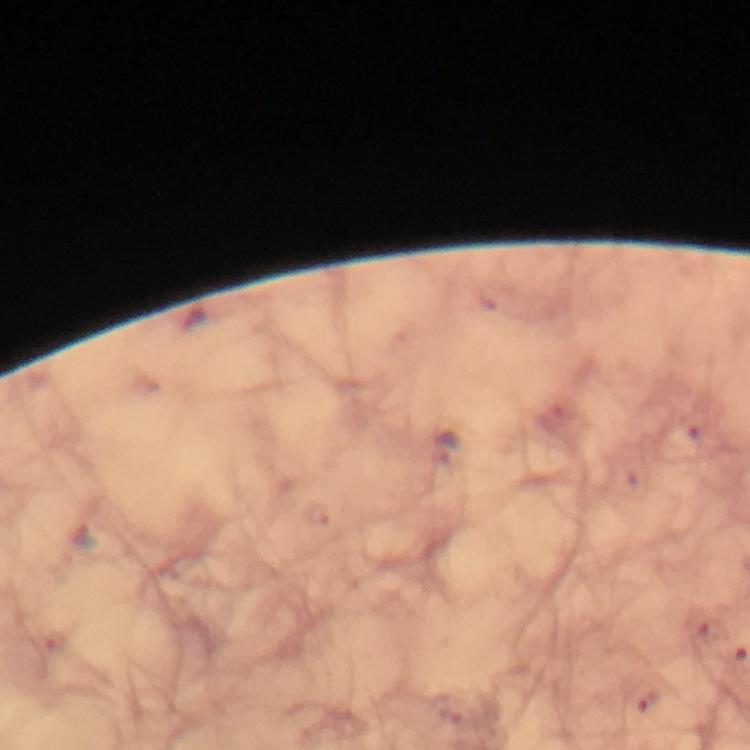

{
  "stain": "Giemsa",
  "magnification": "100x",
  "cropped_from": "one field of view",
  "image_size": "750×750 pixels",
  "plasmodium_parasite_locations": "approximate centers as {x, y} in pixels: {650, 701}",
  "preparation": "thick blood film",
  "immersion_oil": "used",
  "capture": "smartphone photograph through a microscope",
  "context": "from a malaria diagnostic workup"
}